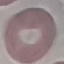
result = no malaria parasites detected
capture = smartphone through the microscope eyepiece
image type = automatically extracted cell patch, resized to 64 × 64 pixels
stain = Giemsa
preparation = thin smear